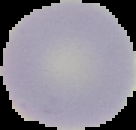
Summary:
  - Preparation: thin blood smear
  - Image type: cell region segmented out of the field of view; surrounding area masked to black
  - Result: no malaria parasites detected
  - Image size: 136×130 pixels